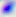
Toxoplasma gondii is seen. Captured at 400x magnification. Micrograph.